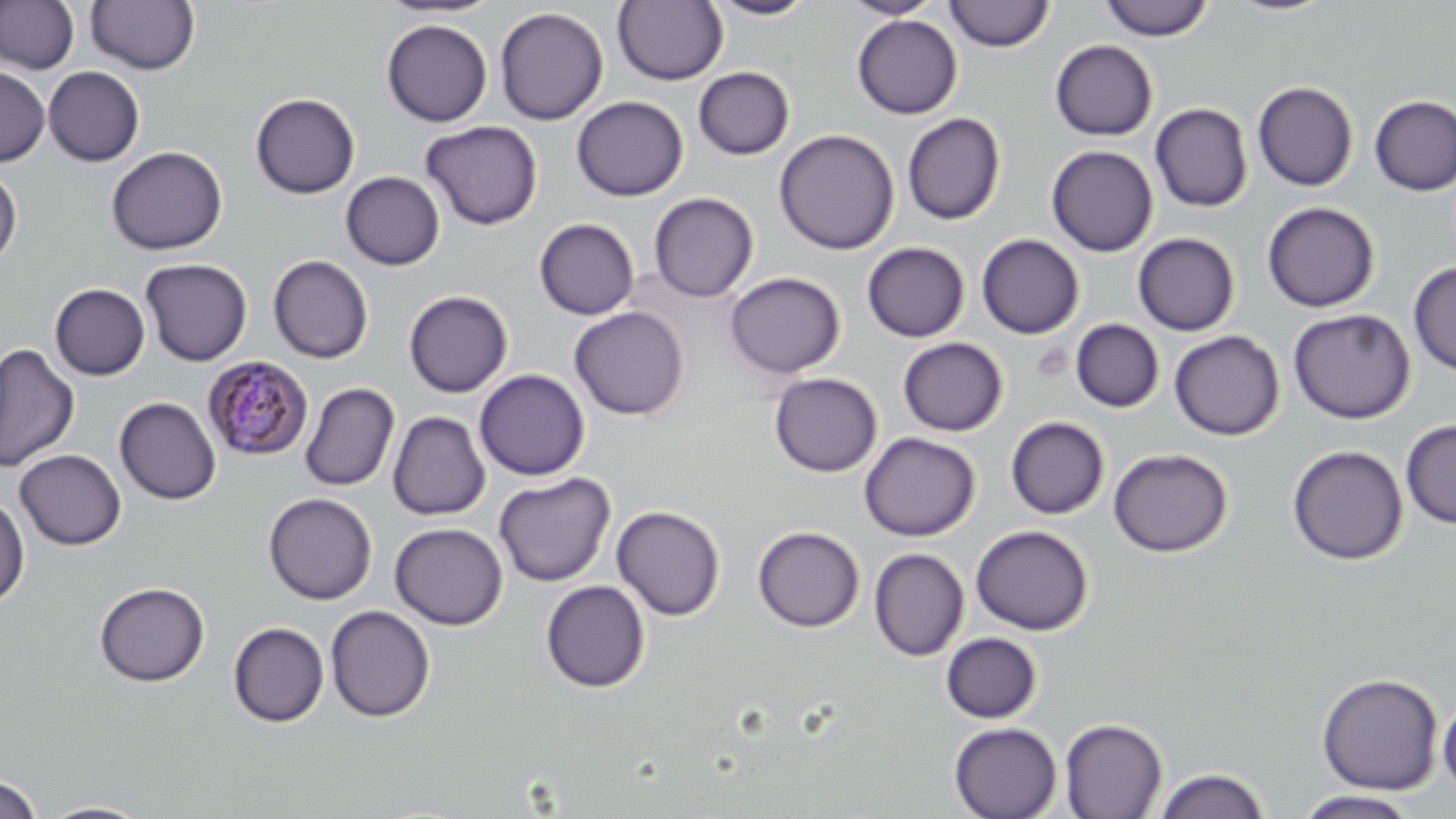

Approximate bounding boxes as [x1, y1, x2, y2] in pixels. Uninfected red blood cell locations: [0, 0, 80, 74], [376, 0, 502, 19], [613, 0, 728, 85], [705, 0, 818, 20], [839, 0, 946, 19], [1099, 0, 1214, 41], [1223, 0, 1338, 16], [86, 1, 201, 74], [944, 1, 1054, 51], [494, 7, 608, 125], [851, 14, 963, 119], [381, 19, 493, 127], [1050, 40, 1158, 141], [0, 66, 50, 166], [43, 66, 145, 166], [693, 67, 795, 160], [1252, 81, 1359, 191], [250, 93, 360, 199], [1370, 95, 1456, 196], [571, 96, 688, 201], [1150, 103, 1253, 212], [902, 112, 1006, 225], [420, 120, 542, 230], [774, 129, 899, 254], [1046, 145, 1158, 257], [106, 146, 227, 255], [0, 167, 22, 267], [340, 171, 445, 270], [649, 192, 759, 303], [1262, 201, 1381, 312], [534, 218, 640, 320], [1133, 232, 1240, 336], [976, 234, 1085, 339], [861, 242, 970, 342], [268, 255, 374, 363], [140, 258, 252, 366], [1408, 262, 1456, 375], [725, 272, 846, 378], [49, 283, 150, 380], [404, 289, 513, 398], [569, 307, 690, 420], [1288, 308, 1416, 424], [1070, 319, 1165, 412], [1169, 330, 1285, 440], [897, 337, 1008, 436], [1, 343, 80, 472], [474, 369, 590, 480], [769, 372, 882, 476], [300, 382, 400, 491], [114, 396, 222, 505], [388, 411, 490, 521], [1005, 416, 1110, 519], [1400, 418, 1456, 529], [859, 432, 980, 541], [1287, 444, 1409, 565], [1108, 447, 1234, 558], [15, 449, 126, 549], [493, 472, 616, 587], [264, 493, 378, 605], [0, 495, 30, 608], [611, 505, 726, 621], [390, 522, 508, 630], [971, 524, 1094, 635], [752, 525, 864, 632], [869, 548, 969, 661], [540, 580, 650, 693], [94, 581, 210, 686], [325, 605, 435, 723], [227, 622, 329, 728], [940, 632, 1042, 723], [1316, 673, 1444, 795], [1437, 693, 1456, 801], [1059, 717, 1168, 818], [948, 722, 1062, 819], [1152, 767, 1271, 819], [0, 774, 42, 818], [1293, 790, 1421, 818], [37, 800, 153, 818]. Plasmodium malariae-infected red blood cell locations: [203, 356, 314, 461]. Slide-level diagnosis: Plasmodium malariae. Light microscopy. 1000x magnification. Single field of view. Thin blood film. Image is 1456×819 pixels. May-Grünwald-Giemsa stain.